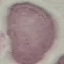
Result: no malaria parasites seen. Giemsa stain. Automatically extracted cell patch, resized to 64 × 64 pixels. Thin smear of blood. Acquired by smartphone through the microscope eyepiece.